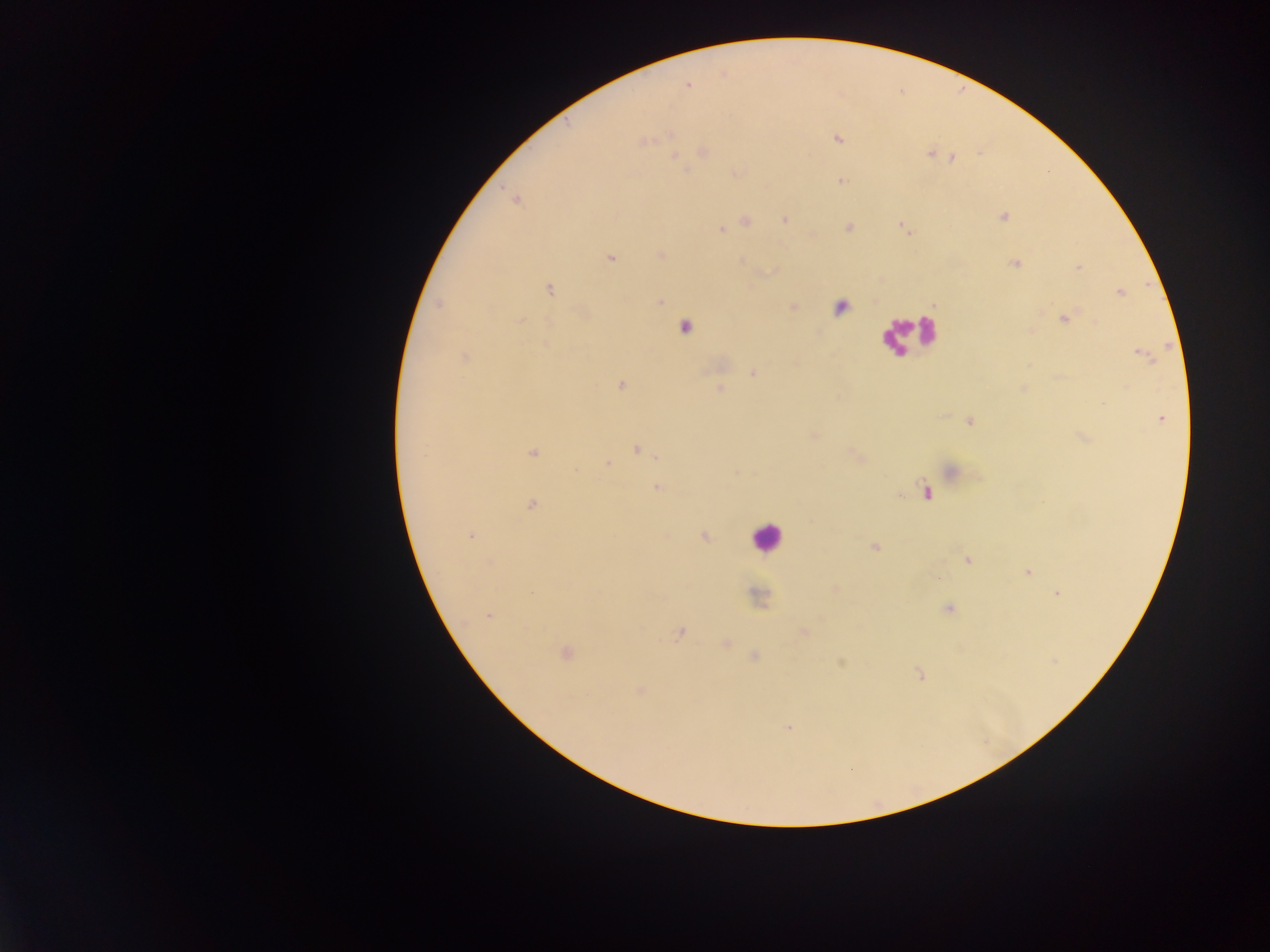

country = Ghana
leukocyte locations = approximate centers as (x, y) in pixels: (907, 334), (765, 536)
field of view = single
malaria parasite locations = approximate centers as (x, y) in pixels: (687, 85), (670, 135), (837, 139), (643, 142), (703, 151), (930, 153), (953, 157), (841, 181), (516, 199), (1003, 217), (784, 219), (745, 221), (848, 227), (722, 229), (661, 255), (611, 258), (1015, 264), (1078, 268), (549, 290), (1119, 293), (660, 302), (439, 304), (1065, 319), (522, 320), (685, 328), (543, 343), (1142, 354), (465, 357), (753, 373), (621, 385), (719, 388), (1102, 403), (1161, 419), (970, 422), (812, 436), (637, 450), (532, 453), (857, 457), (608, 464), (950, 470), (657, 488), (927, 493), (531, 504), (471, 536), (704, 537), (874, 548), (968, 560), (1027, 571), (937, 579), (835, 588), (1057, 594), (948, 609), (488, 616), (679, 633), (805, 634), (726, 643), (566, 653), (754, 656), (841, 664), (918, 674), (640, 691), (788, 728)
image size = 1270×952 pixels
preparation = thick blood smear
capture = mobile-phone photograph through a microscope